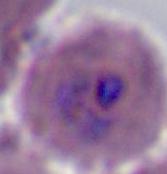
Summary:
  - Identification: Plasmodium
  - Modality: micrograph
  - Magnification: 400x or 1000x